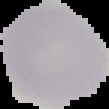
image type = cell region segmented out of the field of view; surrounding area masked to black
image size = 109×109 pixels
preparation = thin blood film
malaria status = uninfected